Comment on the morphology of the erythrocytes.
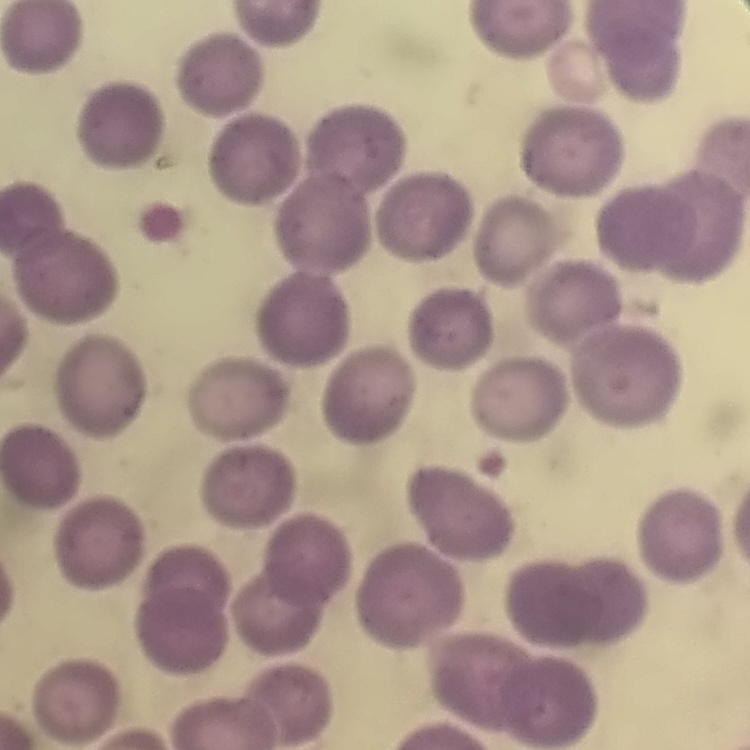
They show no rouleaux formation.

stain = Field's or Giemsa
image type = one tile cut from a larger photomicrograph
preparation = thin peripheral smear